Report the malaria status of this cell.
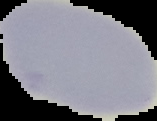

It is uninfected.

Summary:
  - Image type: segmented cell region with the area outside set to black
  - Image size: 157×121 pixels
  - Preparation: thin blood film